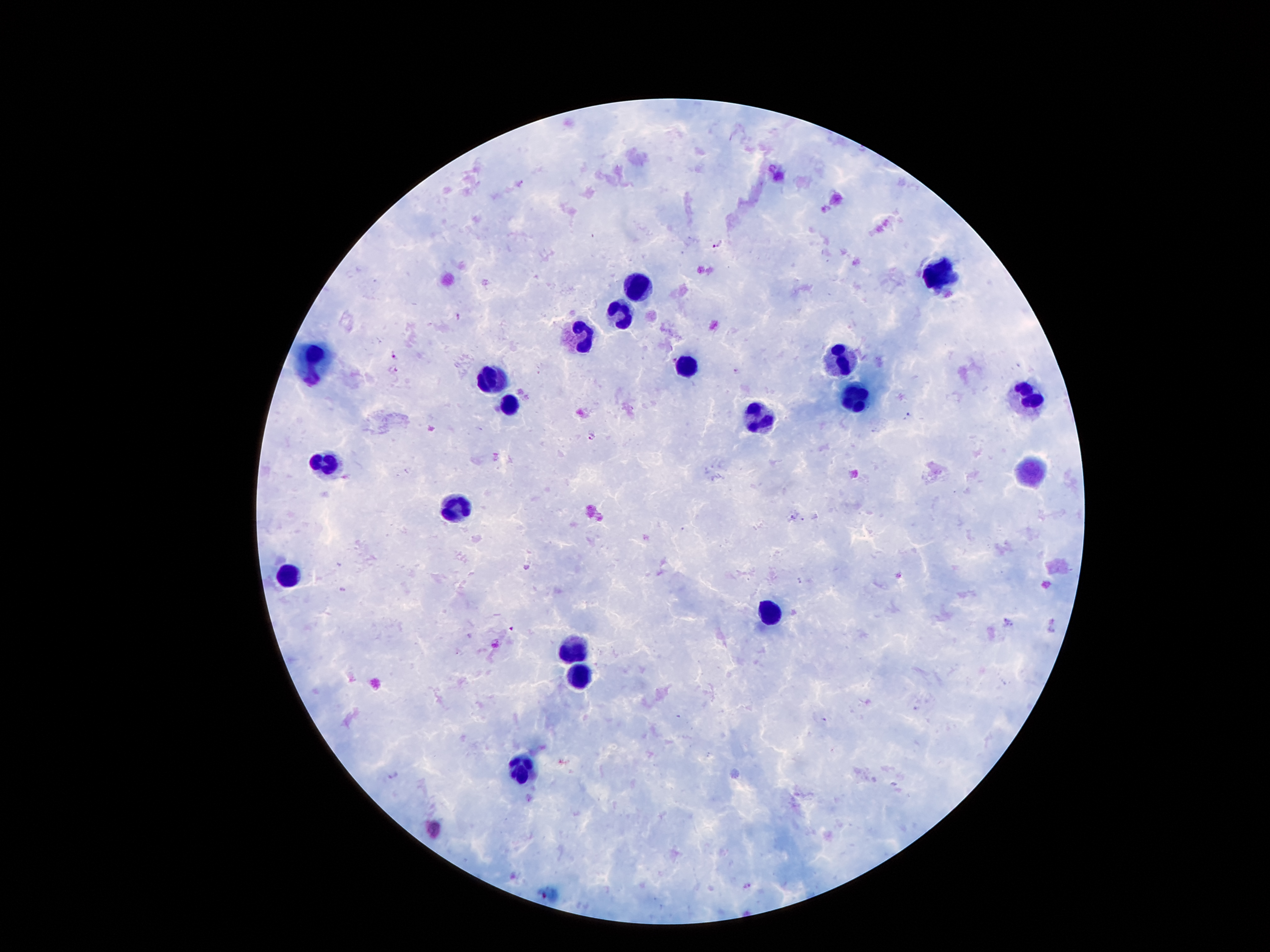

Approximate centers as [x, y] in pixels. Leukocyte locations: [935, 273], [636, 282], [621, 312], [582, 335], [313, 358], [842, 360], [685, 365], [492, 381], [856, 398], [1025, 399], [509, 409], [767, 421], [324, 461], [1026, 472], [459, 510], [283, 575], [769, 612], [575, 648], [580, 676], [520, 773]. Plasmodium parasite locations: [719, 245], [460, 316], [396, 358], [674, 360], [395, 369], [738, 371], [909, 417], [591, 433], [792, 515], [805, 520], [800, 580], [1008, 621], [393, 775]. One field from this slide. Image is 1270×952 pixels. Giemsa-stained preparation. Thick peripheral-blood smear. 100x magnification. Patient malaria status: positive for Plasmodium falciparum. Smartphone photograph taken through the microscope eyepiece.